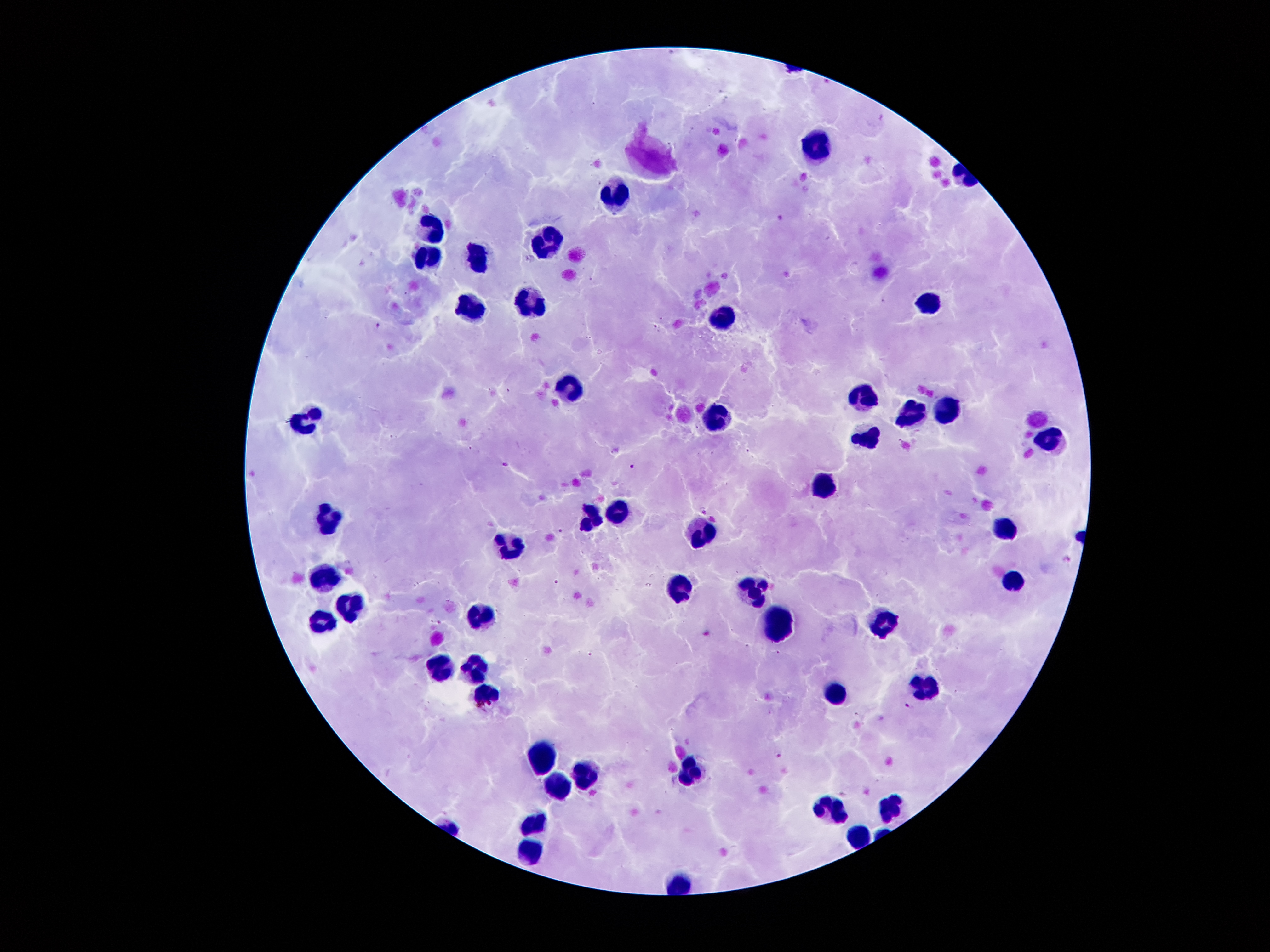 Approximate centers as [x, y] in pixels. Leukocyte locations: [819, 145], [617, 191], [433, 227], [546, 244], [428, 263], [475, 264], [533, 301], [930, 302], [470, 310], [723, 317], [575, 389], [863, 393], [949, 406], [908, 414], [306, 417], [719, 419], [864, 436], [1048, 439], [819, 488], [614, 511], [594, 514], [329, 520], [702, 529], [1000, 529], [512, 549], [325, 577], [1013, 579], [682, 583], [753, 588], [347, 607], [479, 613], [323, 620], [882, 623], [774, 628], [474, 664], [441, 666], [927, 683], [486, 693], [837, 694], [542, 755], [690, 766], [587, 771], [560, 793], [833, 807], [894, 808], [532, 820], [860, 837], [528, 853], [681, 882]. Plasmodium parasite locations: [379, 326], [504, 466], [632, 466], [705, 509], [562, 530], [1069, 560], [556, 581], [589, 654], [906, 704], [778, 755]. 100x magnification. Giemsa stain. One field from this slide. Thick peripheral-blood smear. Patient malaria status: positive for Plasmodium falciparum. Image is 1270×952 pixels. Smartphone photograph taken through the microscope eyepiece.